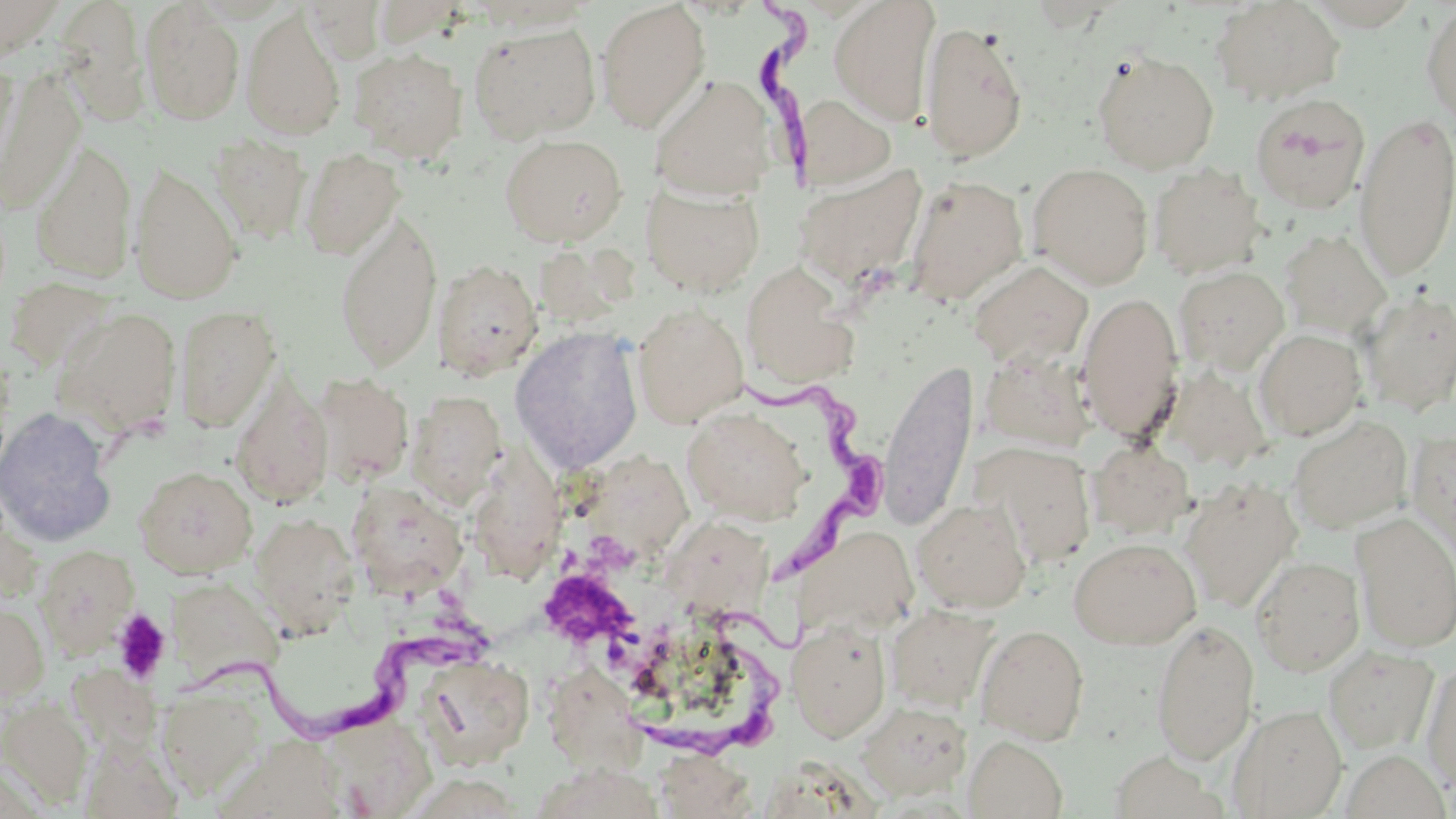
Approximate bounding boxes as named x1/y1/x2/y2 corners in pixels. Platelet locations: (x1=540, y1=570, x2=639, y2=650), (x1=111, y1=609, x2=172, y2=684). Uninfected red blood cell locations: (x1=0, y1=0, x2=68, y2=62), (x1=301, y1=0, x2=387, y2=63), (x1=829, y1=0, x2=940, y2=125), (x1=1211, y1=0, x2=1345, y2=105), (x1=56, y1=1, x2=151, y2=123), (x1=595, y1=1, x2=711, y2=133), (x1=140, y1=2, x2=244, y2=125), (x1=1299, y1=3, x2=1426, y2=30), (x1=1421, y1=3, x2=1456, y2=125), (x1=242, y1=9, x2=346, y2=141), (x1=919, y1=18, x2=1029, y2=163), (x1=468, y1=22, x2=601, y2=143), (x1=349, y1=47, x2=468, y2=163), (x1=1093, y1=50, x2=1220, y2=174), (x1=0, y1=60, x2=19, y2=183), (x1=0, y1=70, x2=86, y2=215), (x1=649, y1=74, x2=777, y2=201), (x1=794, y1=93, x2=897, y2=191), (x1=1250, y1=93, x2=1370, y2=214), (x1=1354, y1=112, x2=1456, y2=281), (x1=208, y1=134, x2=311, y2=244), (x1=499, y1=134, x2=628, y2=246), (x1=30, y1=139, x2=137, y2=283), (x1=299, y1=147, x2=405, y2=261), (x1=130, y1=162, x2=244, y2=304), (x1=793, y1=163, x2=928, y2=291), (x1=1028, y1=163, x2=1153, y2=288), (x1=1149, y1=163, x2=1266, y2=278), (x1=904, y1=174, x2=1029, y2=307), (x1=641, y1=182, x2=765, y2=296), (x1=334, y1=210, x2=443, y2=371), (x1=1279, y1=229, x2=1392, y2=338), (x1=432, y1=258, x2=544, y2=381), (x1=969, y1=259, x2=1093, y2=370), (x1=741, y1=261, x2=858, y2=390), (x1=1173, y1=266, x2=1289, y2=373), (x1=3, y1=276, x2=121, y2=374), (x1=1359, y1=288, x2=1456, y2=417), (x1=1077, y1=291, x2=1184, y2=441), (x1=631, y1=303, x2=749, y2=427), (x1=174, y1=304, x2=281, y2=432), (x1=54, y1=307, x2=181, y2=438), (x1=510, y1=326, x2=645, y2=473), (x1=1254, y1=329, x2=1367, y2=440), (x1=878, y1=358, x2=978, y2=531), (x1=1160, y1=365, x2=1272, y2=471), (x1=313, y1=372, x2=413, y2=487), (x1=230, y1=376, x2=334, y2=508), (x1=407, y1=391, x2=507, y2=508), (x1=0, y1=407, x2=117, y2=547), (x1=683, y1=407, x2=810, y2=526), (x1=1287, y1=416, x2=1413, y2=534), (x1=1407, y1=429, x2=1456, y2=562), (x1=476, y1=439, x2=575, y2=589), (x1=1089, y1=440, x2=1194, y2=538), (x1=974, y1=442, x2=1096, y2=567), (x1=579, y1=443, x2=690, y2=572), (x1=134, y1=466, x2=257, y2=578), (x1=938, y1=474, x2=1071, y2=596), (x1=1181, y1=478, x2=1303, y2=612), (x1=347, y1=481, x2=468, y2=596), (x1=912, y1=498, x2=1031, y2=613), (x1=249, y1=511, x2=359, y2=636), (x1=1351, y1=512, x2=1456, y2=652), (x1=665, y1=518, x2=774, y2=620), (x1=790, y1=524, x2=920, y2=640), (x1=1068, y1=537, x2=1202, y2=649), (x1=35, y1=545, x2=139, y2=656), (x1=1251, y1=555, x2=1365, y2=676), (x1=165, y1=586, x2=275, y2=684), (x1=0, y1=601, x2=50, y2=703), (x1=886, y1=604, x2=999, y2=712), (x1=787, y1=618, x2=892, y2=742), (x1=1151, y1=618, x2=1259, y2=764), (x1=976, y1=624, x2=1089, y2=744), (x1=1323, y1=645, x2=1438, y2=753), (x1=417, y1=653, x2=534, y2=769), (x1=1422, y1=661, x2=1456, y2=793), (x1=542, y1=662, x2=652, y2=781), (x1=159, y1=684, x2=265, y2=798), (x1=1, y1=696, x2=92, y2=806), (x1=858, y1=701, x2=971, y2=799), (x1=1228, y1=704, x2=1347, y2=818), (x1=320, y1=715, x2=437, y2=817), (x1=964, y1=735, x2=1068, y2=819), (x1=654, y1=749, x2=756, y2=818), (x1=1340, y1=751, x2=1452, y2=819), (x1=1109, y1=752, x2=1224, y2=819). Trypanosoma brucei locations: (x1=737, y1=2, x2=837, y2=176), (x1=740, y1=373, x2=889, y2=578), (x1=645, y1=605, x2=819, y2=761), (x1=184, y1=625, x2=480, y2=737). Slide-level diagnosis: Trypanosoma brucei. May-Grünwald-Giemsa-stained preparation. Image is 1456×819 pixels. One field of a larger specimen. Thin blood film. Optical microscopy. Captured at 1000x magnification.